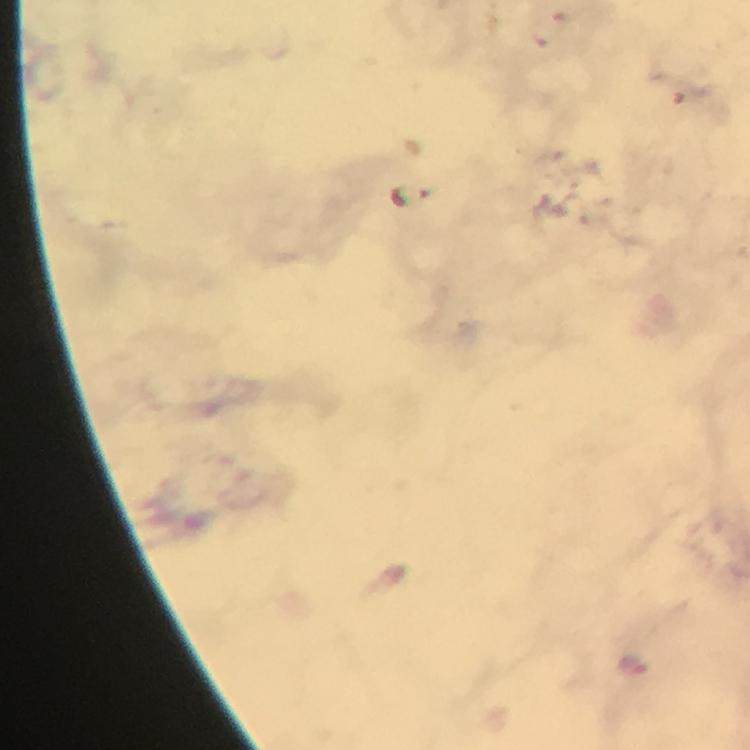 Approximate centers as (x, y) in pixels. Malaria parasite locations: (633, 664). Photographed with a smartphone mounted on the microscope. At 100x magnification. Giemsa stain. Image is 750×750 pixels. A crop from one field of view. Immersion oil applied. From a diagnostic examination for malaria. Thick blood smear.